Give the position of every leukocyte visible.
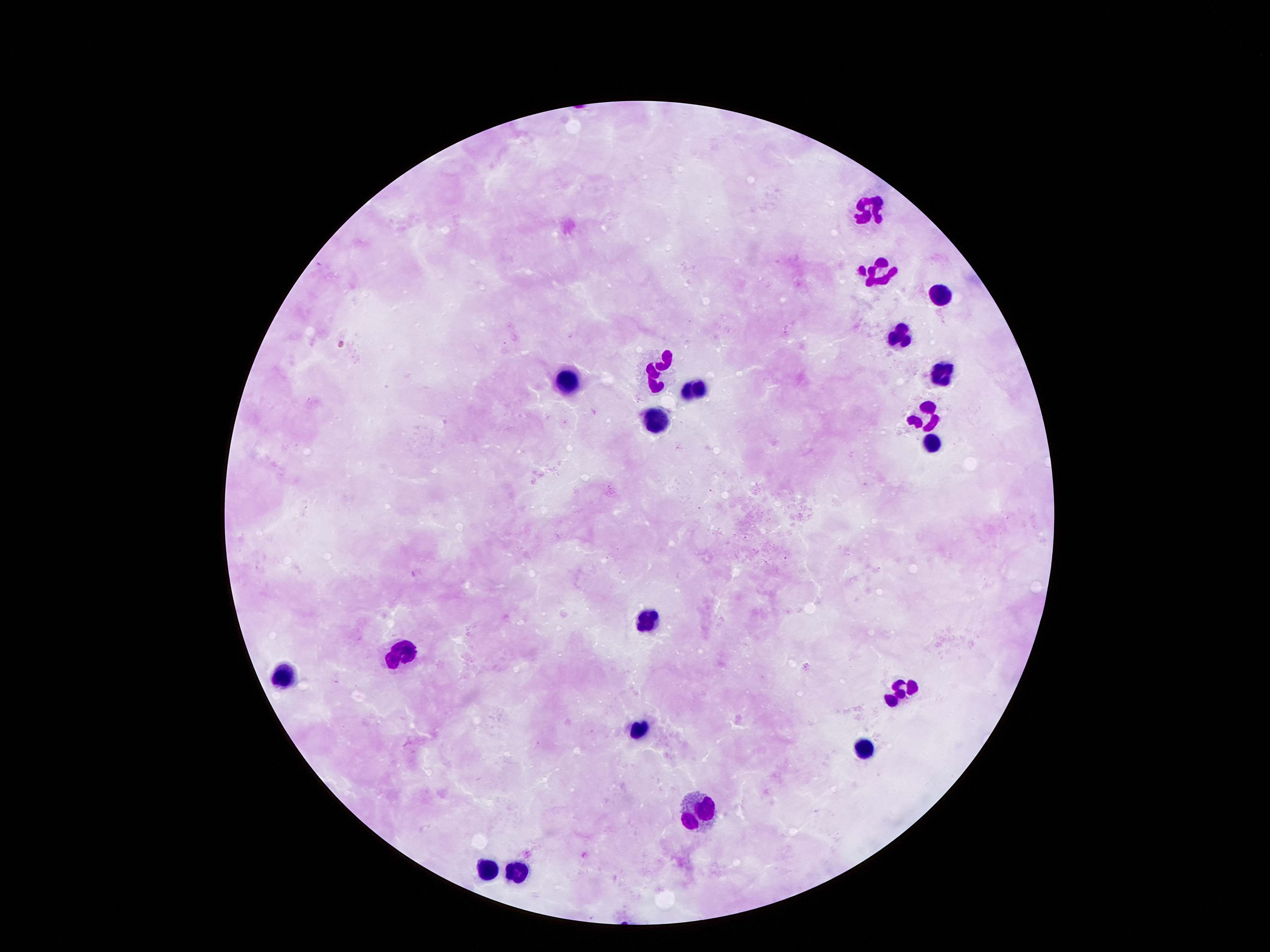
Approximate centers as {x, y} in pixels.
Leukocytes: {871, 206}, {877, 271}, {939, 294}, {898, 330}, {942, 371}, {659, 374}, {692, 387}, {563, 388}, {651, 419}, {922, 420}, {935, 442}, {647, 619}, {396, 652}, {284, 674}, {898, 687}, {634, 731}, {866, 748}, {698, 819}, {488, 868}, {513, 872}.

Summary:
  - Preparation: thick peripheral-blood smear
  - Stain: Giemsa
  - Magnification: 100x
  - Image size: 1270×952 pixels
  - Capture: smartphone camera through the microscope eyepiece
  - Field of view: single
  - Patient malaria status: not infected